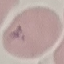

malaria status = parasitized
image type = automatically extracted cell patch, resized to 64 × 64 pixels
preparation = thin blood film
capture = smartphone through the microscope eyepiece
stain = Giemsa